Identify the parasite.
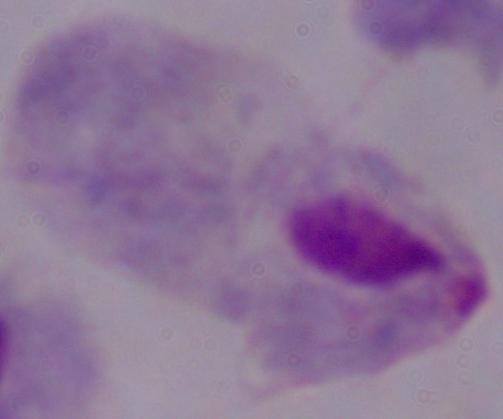

This is a trichomonad.

{
  "modality": "photomicrograph",
  "magnification": "1000x"
}